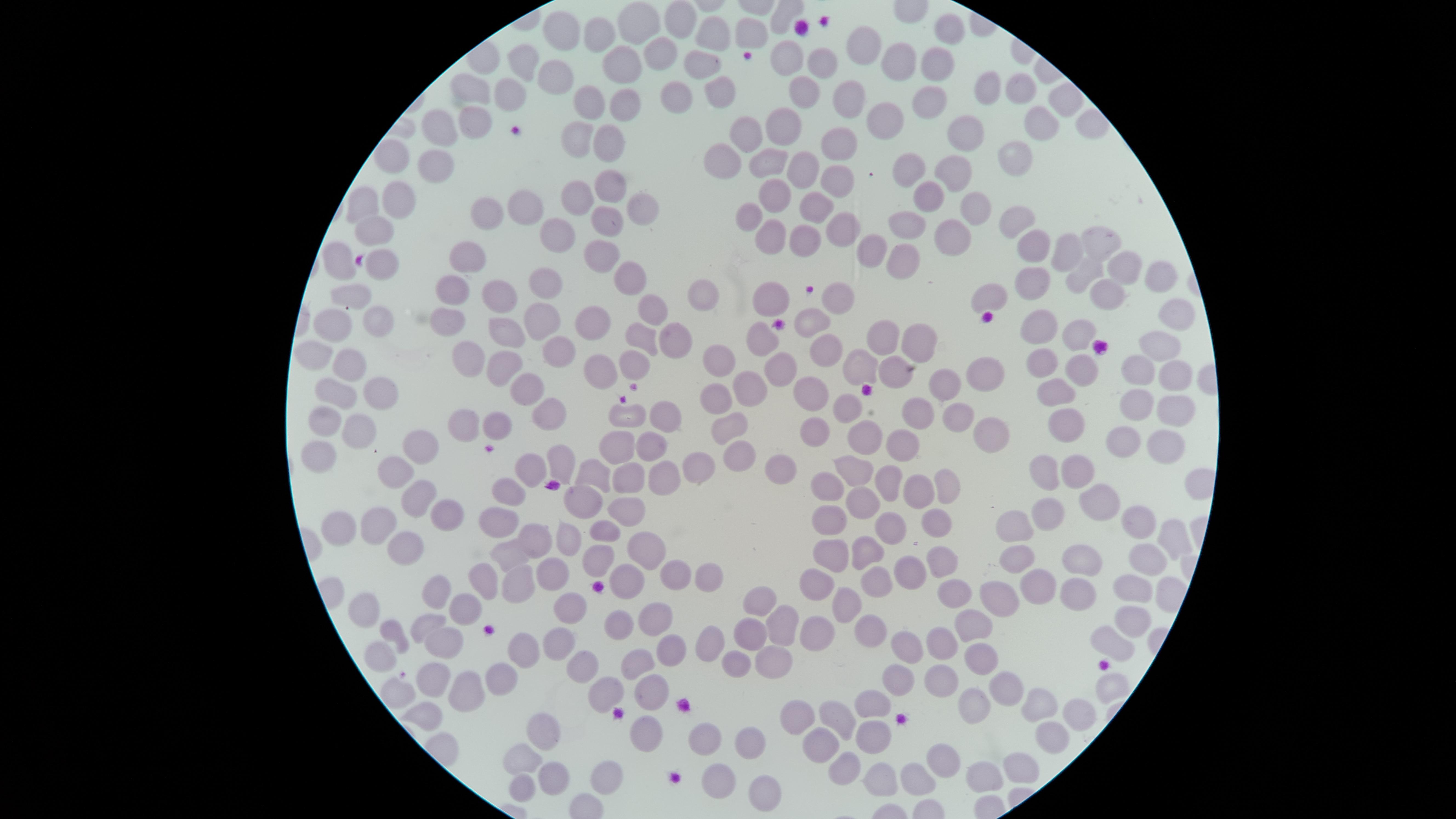

capture = smartphone photograph through the microscope eyepiece
preparation = thin blood film
visible region = circular
field of view = single
presence = no malaria parasites identified
stain = Giemsa
uninfected RBCs = approximate marker points as {x, y} in pixels: {679, 23}, {946, 27}, {562, 31}, {601, 34}, {747, 35}, {712, 40}, {857, 43}, {662, 48}, {788, 57}, {627, 59}, {528, 60}, {818, 61}, {937, 61}, {701, 64}, {898, 66}, {554, 73}, {719, 89}, {795, 90}, {992, 90}, {469, 92}, {1022, 92}, {510, 93}, {852, 96}, {672, 98}, {919, 100}, {1068, 101}, {583, 103}, {622, 109}, {474, 123}, {879, 123}, {1040, 128}, {437, 129}, {783, 129}, {748, 133}, {963, 135}, {574, 136}, {604, 138}, {839, 143}, {727, 151}, {1012, 154}, {392, 160}, {435, 160}, {765, 163}, {799, 165}, {913, 171}, {953, 174}, {837, 182}, {608, 188}, {930, 197}, {398, 200}, {578, 200}, {776, 200}, {361, 204}, {522, 207}, {639, 207}, {969, 208}, {816, 209}, {480, 212}, {1016, 218}, {744, 219}, {606, 222}, {906, 223}, {372, 227}, {839, 228}, {554, 235}, {951, 235}, {800, 239}, {1097, 243}, {1029, 247}, {768, 248}, {875, 249}, {1064, 252}, {469, 255}, {598, 256}, {332, 257}, {899, 260}, {381, 265}, {1120, 269}, {1080, 272}, {620, 276}, {1152, 279}, {1035, 280}, {545, 284}, {449, 288}, {1106, 294}, {990, 295}, {497, 296}, {348, 297}, {692, 297}, {837, 298}, {766, 301}, {1170, 312}, {652, 313}, {370, 318}, {541, 319}, {808, 320}, {593, 322}, {444, 323}, {327, 326}, {1041, 328}, {884, 335}, {1079, 335}, {500, 336}, {916, 337}, {643, 338}, {759, 339}, {674, 341}, {1160, 344}, {559, 345}, {826, 347}, {461, 349}, {317, 354}, {637, 361}, {776, 361}, {717, 362}, {1040, 362}, {505, 364}, {350, 365}, {1076, 368}, {1134, 369}, {887, 370}, {601, 372}, {856, 373}, {984, 373}, {1169, 377}, {940, 386}, {532, 388}, {744, 388}, {1056, 390}, {810, 395}, {382, 396}, {335, 397}, {713, 397}, {1141, 402}, {845, 405}, {548, 409}, {920, 409}, {1179, 411}, {959, 413}, {657, 417}, {621, 420}, {1070, 420}, {730, 421}, {320, 422}, {463, 426}, {495, 427}, {987, 428}, {358, 429}, {814, 430}, {872, 435}, {1123, 441}, {421, 443}, {617, 444}, {652, 444}, {902, 447}, {1161, 448}, {320, 452}, {743, 454}, {1042, 460}, {564, 464}, {780, 467}, {699, 469}, {858, 469}, {531, 471}, {1073, 471}, {396, 472}, {626, 472}, {598, 474}, {663, 478}, {828, 479}, {886, 482}, {942, 482}, {512, 489}, {914, 494}, {1095, 496}, {412, 501}, {582, 501}, {865, 507}, {625, 509}, {444, 514}, {824, 517}, {499, 519}, {1053, 519}, {1138, 523}, {937, 524}, {338, 525}, {380, 526}, {889, 527}, {1011, 529}, {607, 532}, {1172, 535}, {567, 536}, {531, 538}, {636, 544}, {403, 546}, {829, 551}, {860, 551}, {508, 555}, {944, 559}, {1086, 561}, {600, 562}, {1143, 564}, {1017, 565}, {676, 567}, {905, 571}, {552, 572}, {874, 576}, {628, 577}, {706, 578}, {814, 581}, {486, 583}, {1038, 583}, {519, 584}, {1075, 589}, {950, 592}, {1001, 592}, {1130, 593}, {438, 595}, {756, 601}, {845, 602}, {362, 607}, {466, 609}, {572, 610}, {649, 618}, {1131, 618}, {777, 621}, {424, 626}, {618, 627}, {971, 628}, {394, 631}, {872, 631}, {752, 633}, {816, 634}, {1106, 640}, {715, 643}, {938, 643}, {556, 645}, {445, 647}, {667, 648}, {906, 648}, {525, 650}, {381, 653}, {771, 655}, {979, 656}, {638, 662}, {736, 663}, {583, 668}, {435, 674}, {501, 676}, {898, 678}, {937, 680}, {1108, 687}, {1009, 688}, {473, 689}, {398, 690}, {604, 690}, {649, 694}, {874, 699}, {1039, 701}, {971, 705}, {1075, 709}, {425, 710}, {797, 712}, {832, 715}, {731, 726}, {550, 731}, {642, 731}, {879, 733}, {702, 735}, {1046, 735}, {753, 739}, {822, 747}, {520, 762}, {936, 765}, {1014, 767}, {844, 769}, {549, 777}, {601, 777}, {982, 777}, {716, 778}, {879, 780}, {917, 781}, {519, 792}, {766, 792}
image size = 1456×819 pixels